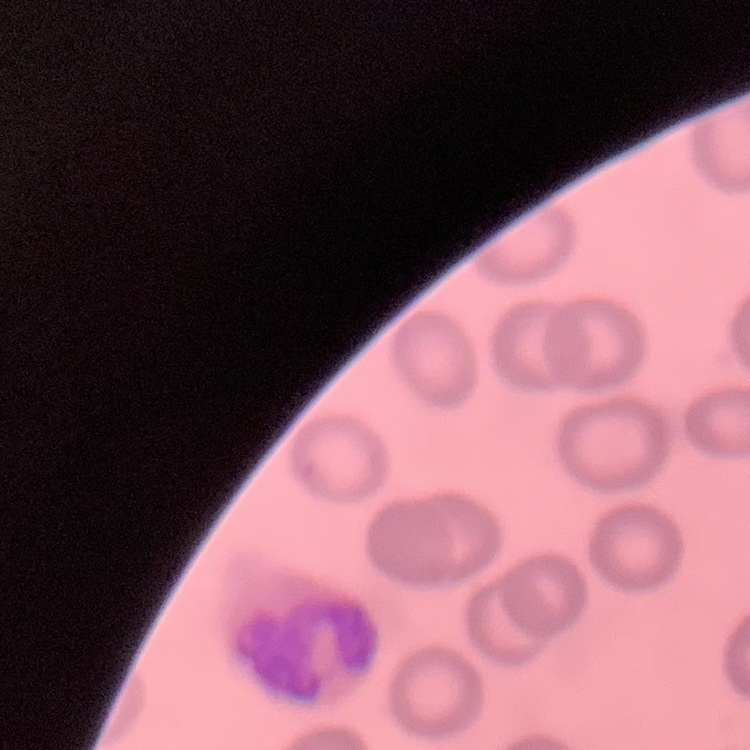

erythrocyte morphology = no rouleaux formation
stain = Field's or Giemsa
image type = square crop of a larger photomicrograph
preparation = thin blood film